Assess the morphology of the erythrocytes.
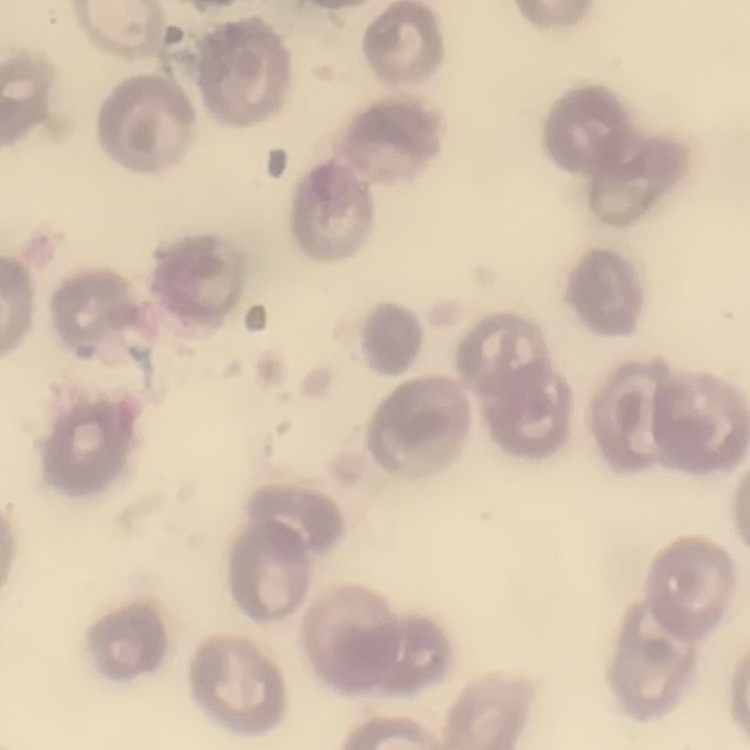

They show no rouleaux formation.

stain = Field's or Giemsa
image type = one tile cut from a larger photomicrograph
preparation = thin blood smear